Point out every malaria parasite.
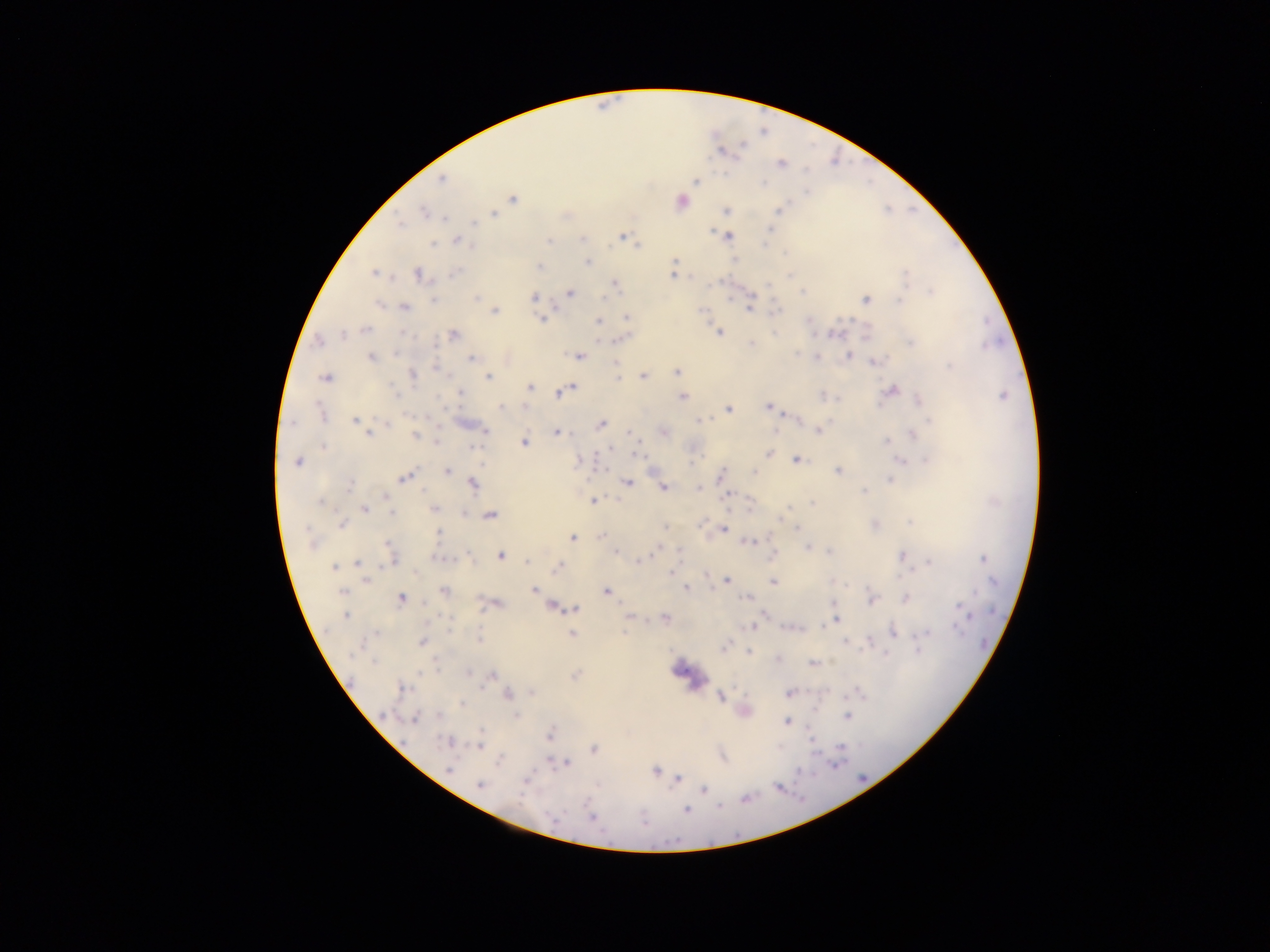

Approximate centers as (x, y) in pixels.
Malaria parasites: (442, 179), (695, 181), (762, 184), (511, 198), (682, 201), (726, 210), (778, 210), (422, 212), (493, 213), (445, 218), (400, 223), (474, 225), (711, 232), (623, 234), (729, 235), (456, 239), (582, 239), (549, 241), (433, 244), (639, 245), (589, 262), (536, 267), (416, 273), (454, 273), (373, 274), (672, 275), (790, 275), (907, 276), (614, 284), (930, 291), (570, 292), (802, 292), (534, 296), (477, 298), (605, 298), (433, 299), (898, 299), (866, 300), (378, 303), (404, 307), (750, 307), (701, 309), (775, 309), (494, 311), (627, 318), (542, 319), (598, 321), (364, 329), (718, 331), (832, 333), (454, 334), (342, 335), (602, 339), (318, 342), (911, 342), (751, 343), (394, 354), (797, 354), (848, 355), (580, 357), (818, 357), (371, 358), (472, 359), (874, 362), (615, 363), (435, 364), (948, 366), (676, 370), (414, 375), (642, 375), (488, 377), (616, 377), (323, 378), (530, 387), (572, 389), (395, 390), (891, 391), (559, 392), (460, 394), (822, 396), (1002, 396), (683, 397), (919, 399), (768, 407), (499, 408), (728, 408), (784, 414), (319, 415), (699, 419), (354, 422), (385, 423), (602, 424), (925, 424), (812, 428), (774, 431), (818, 431), (485, 432), (559, 432), (368, 435), (915, 435), (417, 436), (633, 436), (886, 440), (437, 441), (524, 441), (321, 447), (608, 448), (476, 449), (769, 454), (635, 455), (796, 458), (925, 458), (899, 462), (297, 464), (481, 464), (600, 470), (447, 471), (838, 471), (755, 472), (404, 476), (890, 480), (472, 483), (628, 483), (350, 485), (425, 488), (663, 488), (698, 488), (863, 490), (727, 496), (592, 501), (812, 503), (320, 504), (365, 509), (433, 509), (787, 509), (393, 515), (491, 516), (781, 518), (908, 520), (702, 521), (342, 525), (663, 527), (797, 527), (304, 528), (724, 529), (439, 531), (574, 537), (601, 537), (747, 542), (387, 544), (314, 545), (806, 548), (773, 549), (615, 551), (657, 551), (830, 551), (901, 554), (500, 557), (645, 557), (981, 557), (526, 561), (639, 561), (929, 561), (358, 563), (393, 563), (388, 567), (335, 568), (558, 568), (669, 571), (908, 573), (366, 582), (725, 583), (773, 583), (686, 586), (847, 586), (339, 590), (534, 590), (607, 591), (400, 598), (745, 598), (905, 599), (959, 605), (553, 608), (575, 609), (480, 612), (345, 615), (665, 616), (764, 616), (446, 618), (633, 618), (832, 622), (748, 628), (449, 631), (624, 631), (958, 631), (893, 632), (374, 633), (572, 633), (925, 633), (479, 638), (845, 641), (422, 643), (724, 647), (917, 649), (749, 651), (355, 652), (885, 655), (374, 663), (814, 663), (436, 667), (470, 673), (494, 675), (484, 685), (401, 687), (790, 693), (507, 695), (530, 695), (720, 697), (461, 703), (813, 708), (386, 715), (516, 715), (439, 717), (846, 717), (415, 718), (787, 722), (477, 729), (448, 742), (811, 744), (841, 746), (479, 747), (593, 748), (567, 764), (836, 765), (448, 768), (657, 772), (677, 779), (480, 786), (703, 788), (718, 807), (687, 810), (554, 815), (592, 816), (643, 822).

capture = mobile-phone photograph through a microscope
field of view = single
preparation = thick blood film
image size = 1270×952 pixels
country = Ghana